State the preparation type.
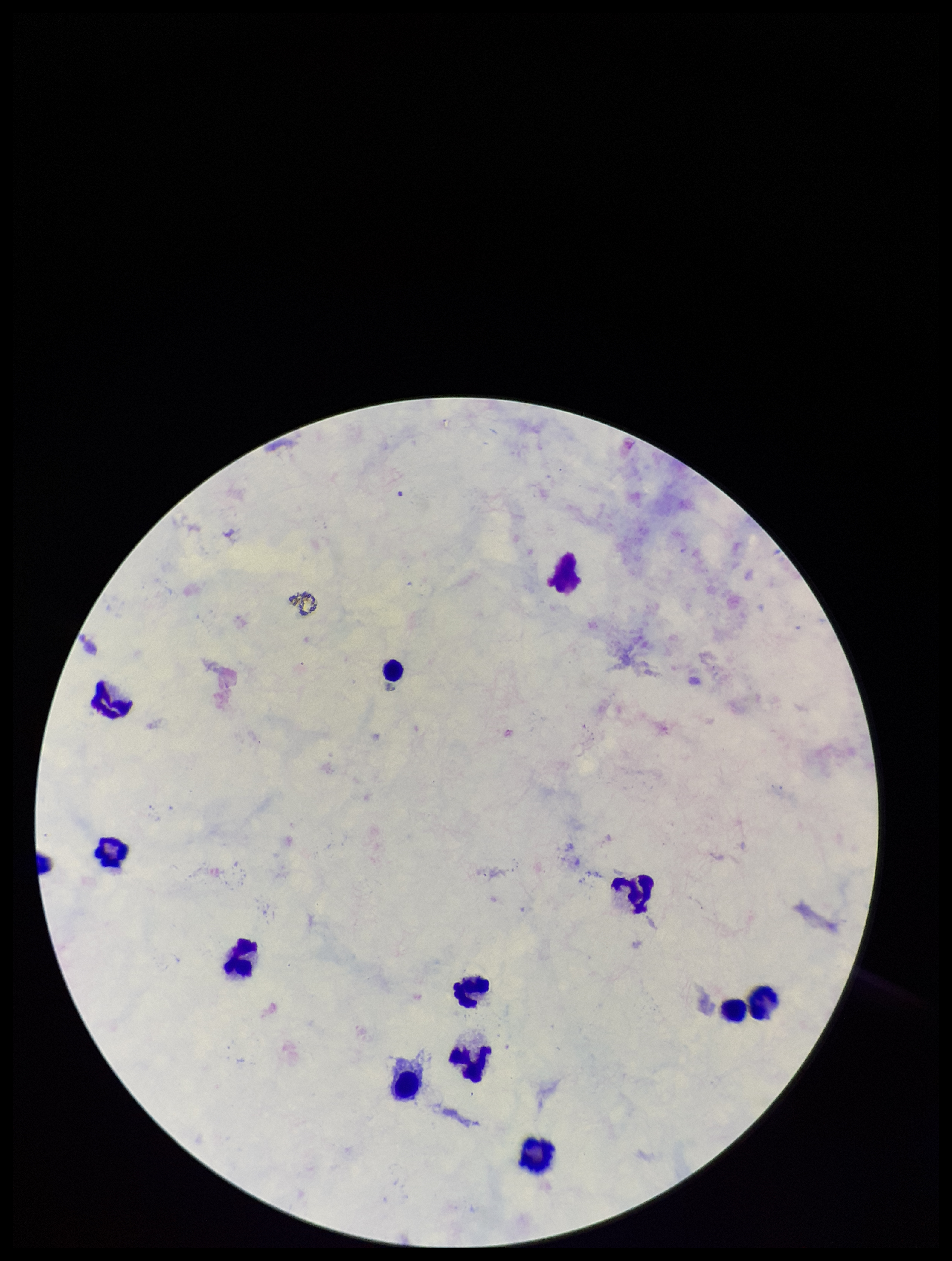

A thick smear.

species reported for this patient = Plasmodium falciparum
Plasmodium parasites = none detected
stain = Giemsa
field of view = single
image size = 952×1261 pixels
leukocyte count = 11
capture = smartphone photograph through the microscope eyepiece
patient malaria status = infected
parasite count = 0